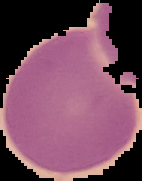
Image is 142×181 pixels. The area outside the segmented cell region is set to black. From a thin blood film. Result: no Plasmodium parasites seen.